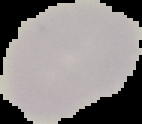

Summary:
  - Image size: 142×124 pixels
  - Preparation: thin blood smear
  - Malaria status: uninfected
  - Image type: segmented cell region on a black background